Classify this cell by malaria status.
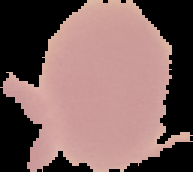

It is uninfected.

{
  "image_size": "193×172 pixels",
  "image_type": "segmented cell region with the area outside set to black",
  "preparation": "thin blood smear"
}